Report the malaria status of this cell.
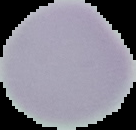
Uninfected.

Summary:
  - Preparation: thin blood film
  - Image size: 136×130 pixels
  - Image type: cell region segmented out of the field of view; surrounding area masked to black